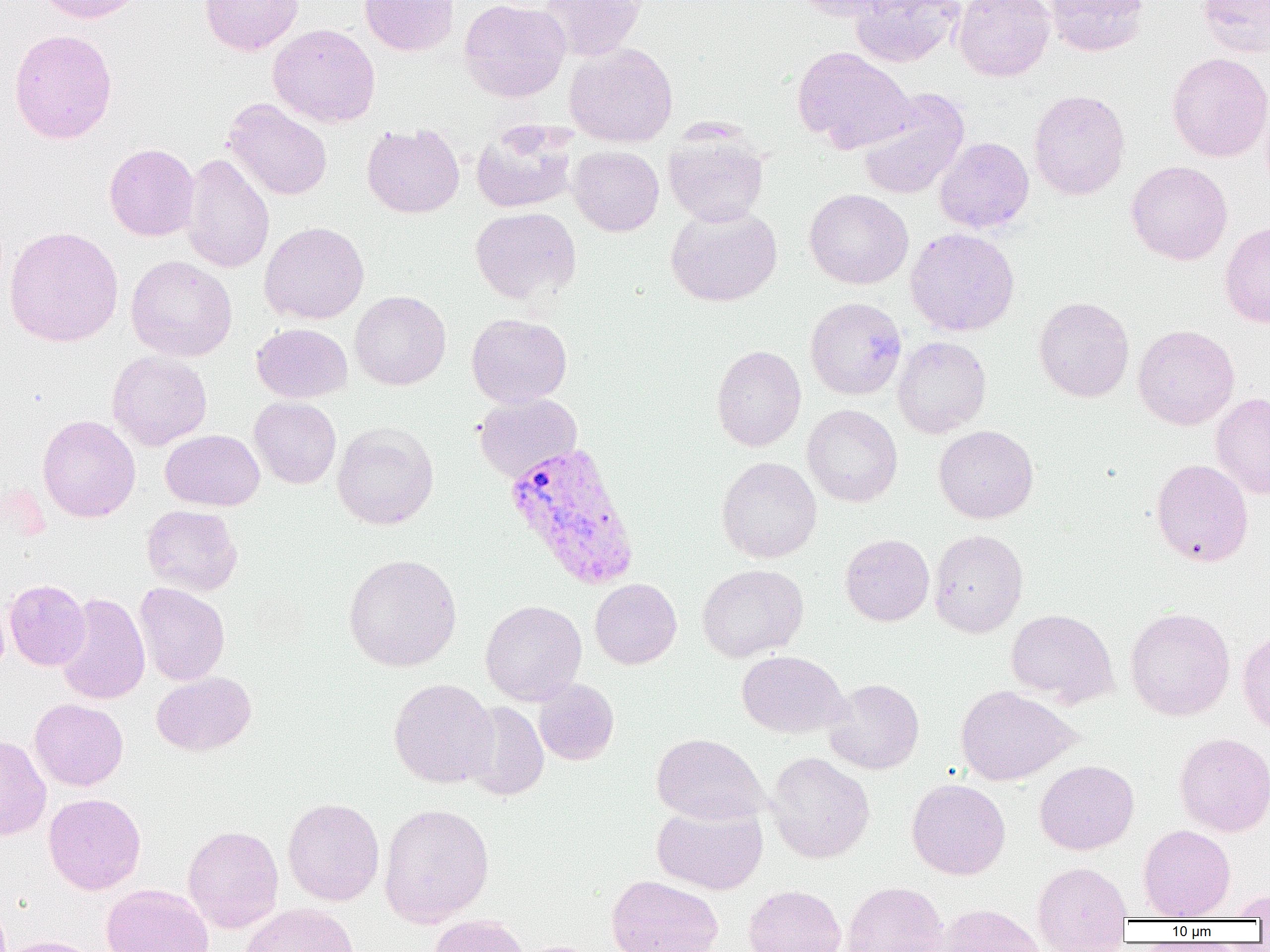
Approximate bounding boxes as [x1, y1, x2, y2] in pixels. Uninfected red blood cell locations: [36, 0, 146, 24], [200, 0, 303, 55], [360, 0, 459, 56], [459, 0, 571, 103], [539, 0, 644, 61], [787, 0, 906, 21], [849, 0, 965, 67], [953, 0, 1055, 81], [1044, 0, 1149, 57], [1197, 0, 1270, 58], [268, 24, 381, 128], [9, 28, 118, 144], [564, 42, 678, 146], [792, 46, 916, 153], [1166, 52, 1270, 162], [856, 88, 970, 200], [1028, 89, 1130, 200], [223, 98, 333, 201], [471, 121, 578, 214], [361, 123, 465, 218], [664, 130, 769, 227], [934, 137, 1034, 234], [104, 143, 200, 241], [567, 145, 664, 236], [181, 153, 274, 274], [1126, 161, 1232, 265], [804, 188, 913, 289], [665, 206, 782, 307], [470, 207, 582, 305], [1220, 221, 1270, 329], [259, 222, 369, 324], [3, 226, 124, 347], [905, 227, 1020, 337], [126, 255, 237, 361], [350, 290, 451, 390], [1033, 296, 1135, 402], [804, 297, 907, 400], [466, 313, 572, 408], [251, 323, 352, 403], [1133, 324, 1240, 430], [892, 336, 991, 438], [711, 345, 806, 452], [107, 351, 212, 451], [1211, 392, 1270, 499], [473, 393, 582, 482], [249, 396, 342, 489], [803, 404, 903, 507], [37, 415, 140, 522], [332, 422, 439, 530], [933, 425, 1038, 524], [160, 429, 264, 511], [716, 456, 822, 563], [1151, 458, 1253, 567], [142, 504, 243, 596], [928, 529, 1028, 638], [840, 534, 934, 626], [343, 553, 462, 672], [697, 564, 808, 662], [590, 578, 682, 669], [4, 579, 90, 670], [134, 582, 230, 686], [54, 592, 150, 705], [480, 599, 587, 706], [1125, 607, 1235, 721], [1006, 608, 1118, 707], [1237, 626, 1270, 738], [736, 650, 848, 739], [151, 671, 256, 756], [388, 677, 499, 788], [823, 678, 925, 775], [533, 679, 619, 765], [955, 684, 1079, 786], [29, 698, 128, 791], [461, 701, 549, 801], [651, 732, 768, 825], [1173, 732, 1270, 837], [0, 733, 51, 841], [766, 752, 875, 863], [1035, 760, 1139, 855], [907, 778, 1010, 880], [43, 793, 146, 895], [282, 797, 384, 906], [379, 802, 495, 928], [652, 802, 768, 895], [182, 824, 284, 933], [1138, 824, 1235, 920], [1032, 861, 1132, 948], [606, 874, 724, 952], [842, 881, 948, 952], [101, 883, 214, 952], [744, 884, 846, 952], [1225, 890, 1270, 920], [240, 903, 360, 952], [934, 903, 1046, 952], [429, 914, 530, 952], [0, 935, 102, 952]. Plasmodium vivax-infected red blood cell locations: [505, 441, 640, 590]. Slide-level diagnosis: Plasmodium vivax. Image is 1270×952 pixels. Single field of view. Light microscopy. Thin blood smear. 1000x magnification.